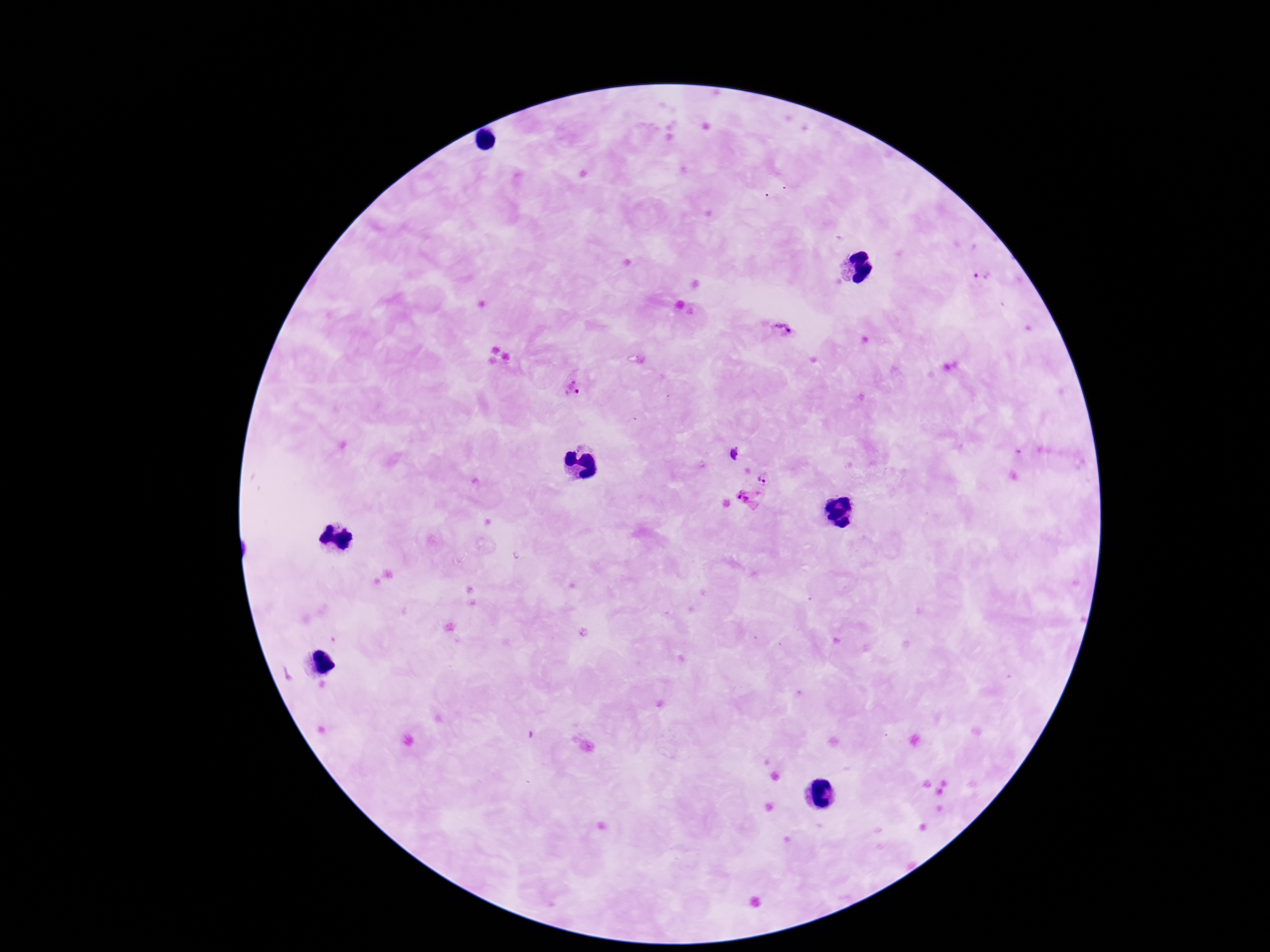

Approximate centers as (x, y) in pixels. Plasmodium parasite locations: (985, 276), (783, 332), (577, 390), (732, 453), (764, 478), (745, 500). Thick peripheral-blood smear. Patient malaria status: positive. 100x magnification. One field from this slide. Smartphone photograph taken through the microscope eyepiece. Image is 1270×952 pixels. Giemsa stain.